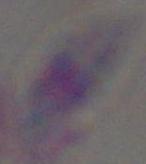
identification = Toxoplasma gondii
modality = micrograph
magnification = 1000x